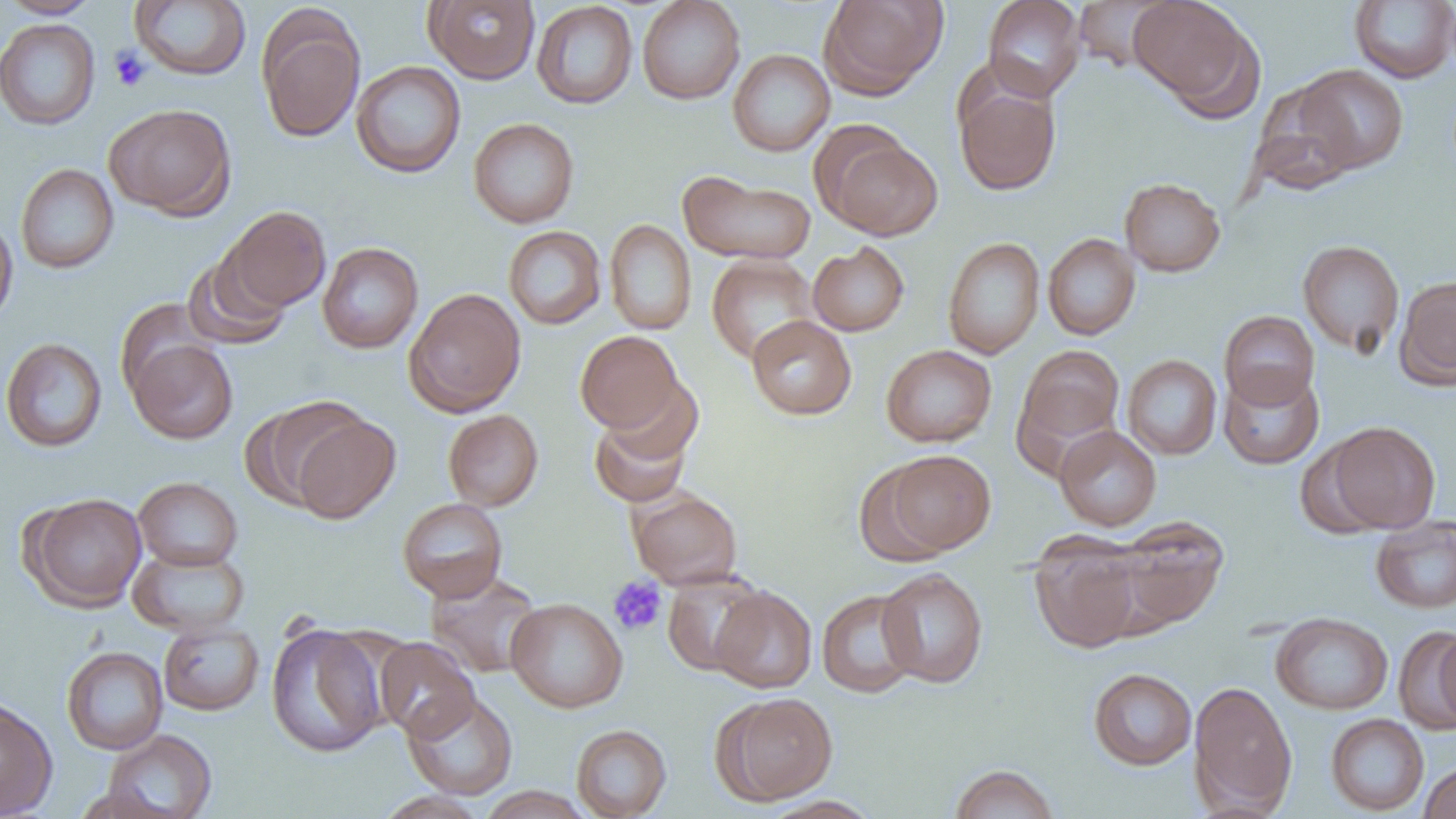 Approximate bounding boxes as named x1/y1/x2/y2 corners in pixels. Uninfected red blood cell locations: (x1=2, y1=0, x2=102, y2=19), (x1=424, y1=0, x2=540, y2=84), (x1=637, y1=0, x2=745, y2=105), (x1=819, y1=0, x2=947, y2=99), (x1=983, y1=0, x2=1085, y2=101), (x1=1129, y1=0, x2=1256, y2=112), (x1=1349, y1=0, x2=1456, y2=84), (x1=130, y1=1, x2=251, y2=80), (x1=531, y1=1, x2=638, y2=109), (x1=1071, y1=1, x2=1177, y2=73), (x1=257, y1=8, x2=365, y2=143), (x1=0, y1=18, x2=101, y2=131), (x1=728, y1=49, x2=835, y2=157), (x1=351, y1=60, x2=466, y2=178), (x1=1294, y1=65, x2=1408, y2=174), (x1=954, y1=81, x2=1062, y2=196), (x1=1250, y1=82, x2=1360, y2=195), (x1=104, y1=103, x2=236, y2=220), (x1=468, y1=118, x2=579, y2=228), (x1=823, y1=135, x2=942, y2=241), (x1=15, y1=163, x2=118, y2=273), (x1=678, y1=170, x2=816, y2=265), (x1=1119, y1=177, x2=1226, y2=277), (x1=223, y1=206, x2=331, y2=312), (x1=0, y1=215, x2=18, y2=328), (x1=604, y1=219, x2=697, y2=335), (x1=503, y1=225, x2=606, y2=329), (x1=1043, y1=234, x2=1141, y2=340), (x1=943, y1=237, x2=1045, y2=359), (x1=1297, y1=239, x2=1405, y2=357), (x1=807, y1=241, x2=910, y2=336), (x1=317, y1=242, x2=423, y2=353), (x1=183, y1=249, x2=292, y2=350), (x1=706, y1=255, x2=819, y2=363), (x1=1395, y1=275, x2=1456, y2=389), (x1=404, y1=288, x2=526, y2=417), (x1=114, y1=298, x2=214, y2=399), (x1=1219, y1=310, x2=1319, y2=409), (x1=746, y1=315, x2=856, y2=420), (x1=575, y1=331, x2=683, y2=432), (x1=1, y1=337, x2=108, y2=453), (x1=127, y1=339, x2=239, y2=444), (x1=881, y1=344, x2=997, y2=447), (x1=1016, y1=345, x2=1125, y2=451), (x1=1122, y1=354, x2=1222, y2=459), (x1=1218, y1=367, x2=1324, y2=469), (x1=588, y1=397, x2=698, y2=509), (x1=245, y1=399, x2=365, y2=509), (x1=443, y1=409, x2=543, y2=511), (x1=291, y1=413, x2=400, y2=524), (x1=1325, y1=421, x2=1442, y2=533), (x1=1054, y1=425, x2=1162, y2=531), (x1=880, y1=450, x2=996, y2=556), (x1=854, y1=462, x2=955, y2=566), (x1=133, y1=476, x2=243, y2=571), (x1=629, y1=489, x2=743, y2=589), (x1=24, y1=492, x2=147, y2=611), (x1=397, y1=498, x2=508, y2=602), (x1=1370, y1=515, x2=1456, y2=614), (x1=1112, y1=517, x2=1228, y2=630), (x1=1031, y1=540, x2=1145, y2=654), (x1=128, y1=545, x2=249, y2=638), (x1=877, y1=568, x2=988, y2=688), (x1=425, y1=571, x2=544, y2=678), (x1=662, y1=571, x2=767, y2=676), (x1=711, y1=586, x2=817, y2=693), (x1=817, y1=589, x2=922, y2=698), (x1=505, y1=597, x2=628, y2=713), (x1=1271, y1=612, x2=1393, y2=715), (x1=158, y1=621, x2=264, y2=716), (x1=266, y1=622, x2=388, y2=758), (x1=1395, y1=627, x2=1456, y2=731), (x1=1433, y1=628, x2=1456, y2=729), (x1=374, y1=638, x2=479, y2=742), (x1=61, y1=646, x2=168, y2=754), (x1=1088, y1=668, x2=1197, y2=770), (x1=1189, y1=681, x2=1298, y2=814), (x1=403, y1=691, x2=518, y2=800), (x1=718, y1=692, x2=837, y2=804), (x1=0, y1=698, x2=58, y2=817), (x1=1326, y1=713, x2=1429, y2=816), (x1=571, y1=724, x2=671, y2=818), (x1=101, y1=729, x2=217, y2=818), (x1=1419, y1=761, x2=1456, y2=818), (x1=948, y1=763, x2=1060, y2=819), (x1=476, y1=786, x2=594, y2=819), (x1=373, y1=791, x2=491, y2=819), (x1=758, y1=796, x2=883, y2=819). Platelet locations: (x1=109, y1=45, x2=152, y2=91), (x1=607, y1=576, x2=668, y2=636). Slide-level diagnosis: no evidence of blood parasites. Image is 1456×819 pixels. One field of a larger specimen. Light microscopy. 1000x magnification. Thin blood film.